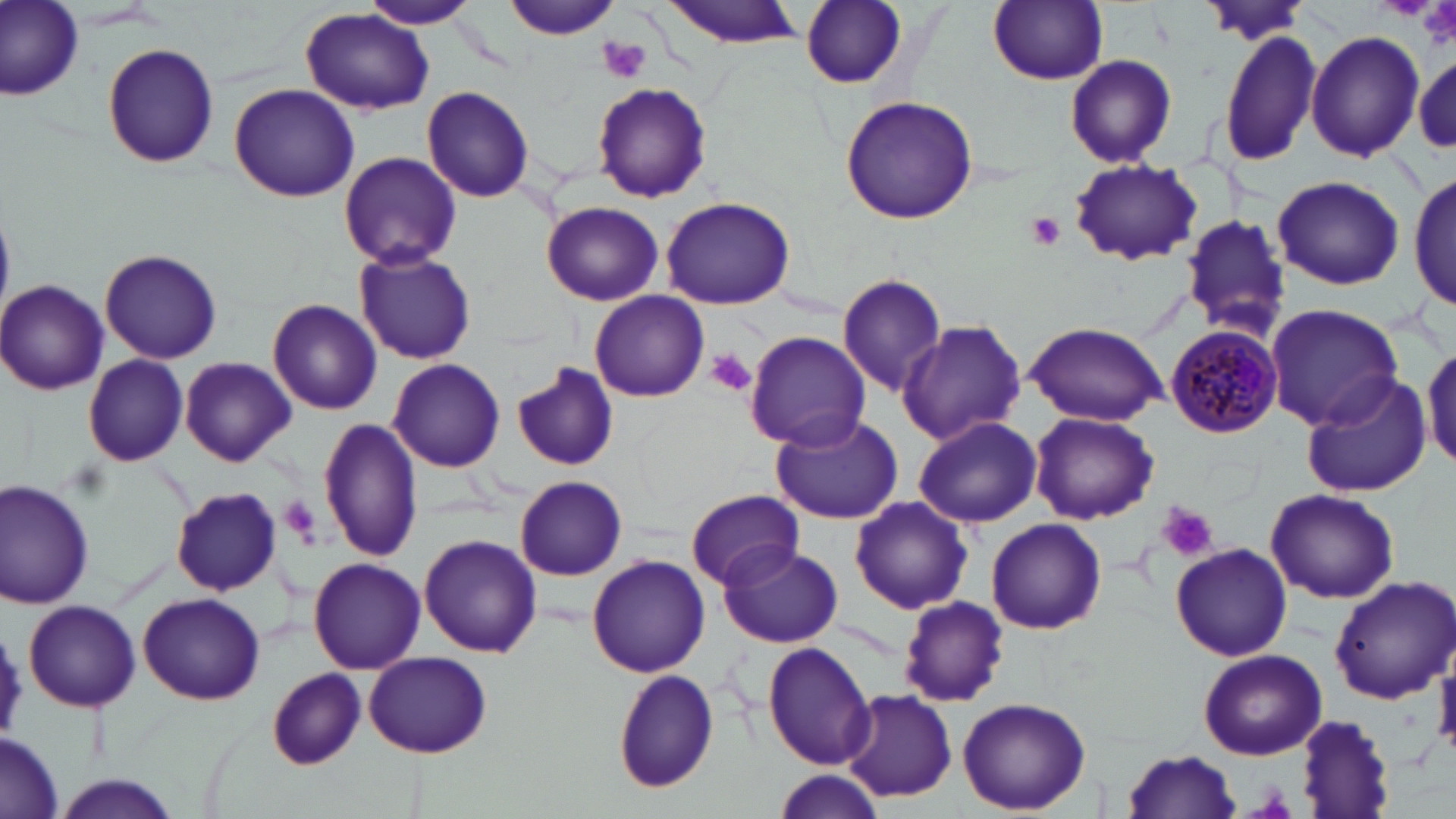

{
  "plasmodium_malariae_infected_red_blood_cell_locations": "approximate bounding boxes as (x1,y1)-(x2,y2) corner pairs in pixels: (1164,324)-(1283,439)",
  "slide_level_diagnosis": "Plasmodium malariae",
  "field_of_view": "one of a larger specimen",
  "platelet_locations": "approximate bounding boxes as (x1,y1)-(x2,y2) corner pairs in pixels: (1420,0)-(1456,49), (597,37)-(650,83), (1024,211)-(1067,252), (707,350)-(759,398), (279,497)-(321,543), (1157,503)-(1217,561)",
  "magnification": "1000x",
  "uninfected_red_blood_cell_locations": "approximate bounding boxes as (x1,y1)-(x2,y2) corner pairs in pixels: (358,0)-(481,30), (503,0)-(620,42), (658,0)-(812,50), (988,0)-(1107,86), (1192,0)-(1314,48), (2,1)-(83,103), (801,1)-(908,88), (301,7)-(435,115), (1217,28)-(1323,167), (1306,29)-(1424,163), (101,43)-(220,170), (1064,54)-(1177,168), (1413,55)-(1456,151), (592,82)-(711,203), (229,83)-(360,203), (422,86)-(535,203), (840,97)-(977,227), (339,151)-(462,270), (1067,159)-(1204,267), (1410,167)-(1456,314), (1271,174)-(1405,291), (661,196)-(796,311), (542,202)-(663,306), (1175,212)-(1292,340), (353,247)-(477,365), (99,248)-(223,364), (837,274)-(948,396), (1,280)-(108,395), (588,290)-(709,403), (268,300)-(382,415), (1263,304)-(1405,429), (896,320)-(1027,446), (1023,322)-(1170,425), (743,331)-(872,451), (1422,341)-(1456,472), (84,353)-(188,467), (182,358)-(296,465), (389,359)-(505,470), (512,362)-(618,472), (1300,375)-(1430,498), (1030,412)-(1160,524), (769,413)-(904,525), (318,414)-(422,564), (914,416)-(1042,528), (515,475)-(628,581), (0,480)-(95,611), (1265,487)-(1400,604), (172,488)-(284,595), (687,488)-(804,590), (848,497)-(973,616), (986,517)-(1108,635), (418,534)-(542,657), (1170,541)-(1292,661), (718,543)-(842,649), (587,555)-(710,678), (307,557)-(426,674), (1326,575)-(1456,703), (139,592)-(264,705), (897,595)-(1011,708), (23,599)-(141,712), (0,627)-(29,736), (762,642)-(876,771), (1199,649)-(1328,761), (364,650)-(492,758), (775,664)-(934,791), (611,668)-(721,794), (267,670)-(366,769), (841,687)-(957,803), (956,697)-(1092,815), (1294,715)-(1396,818), (0,734)-(63,819), (1118,749)-(1245,818), (772,769)-(879,819), (52,773)-(186,819)",
  "image_size": "1456×819 pixels",
  "modality": "optical microscopy",
  "preparation": "thin blood film",
  "stain": "May-Grünwald-Giemsa"
}